Assess this cell for malaria.
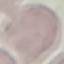
Uninfected.

Cell patch, automatically extracted from a larger field of view and resized to 64 × 64 pixels. Giemsa stain. Thin blood smear. Acquired by smartphone through the microscope eyepiece.